Identify the parasite.
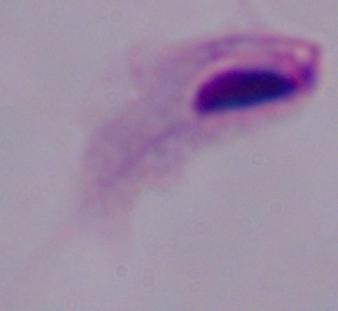
A trichomonad.

magnification = 1000x
modality = photomicrograph